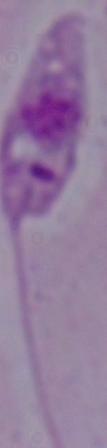
A Leishmania parasite is shown. Captured at 1000x magnification. Photomicrograph.